Classify this cell by malaria status.
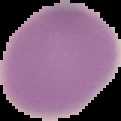
It is uninfected.

image size = 121×121 pixels
image type = segmented cell region with the area outside set to black
preparation = thin blood film